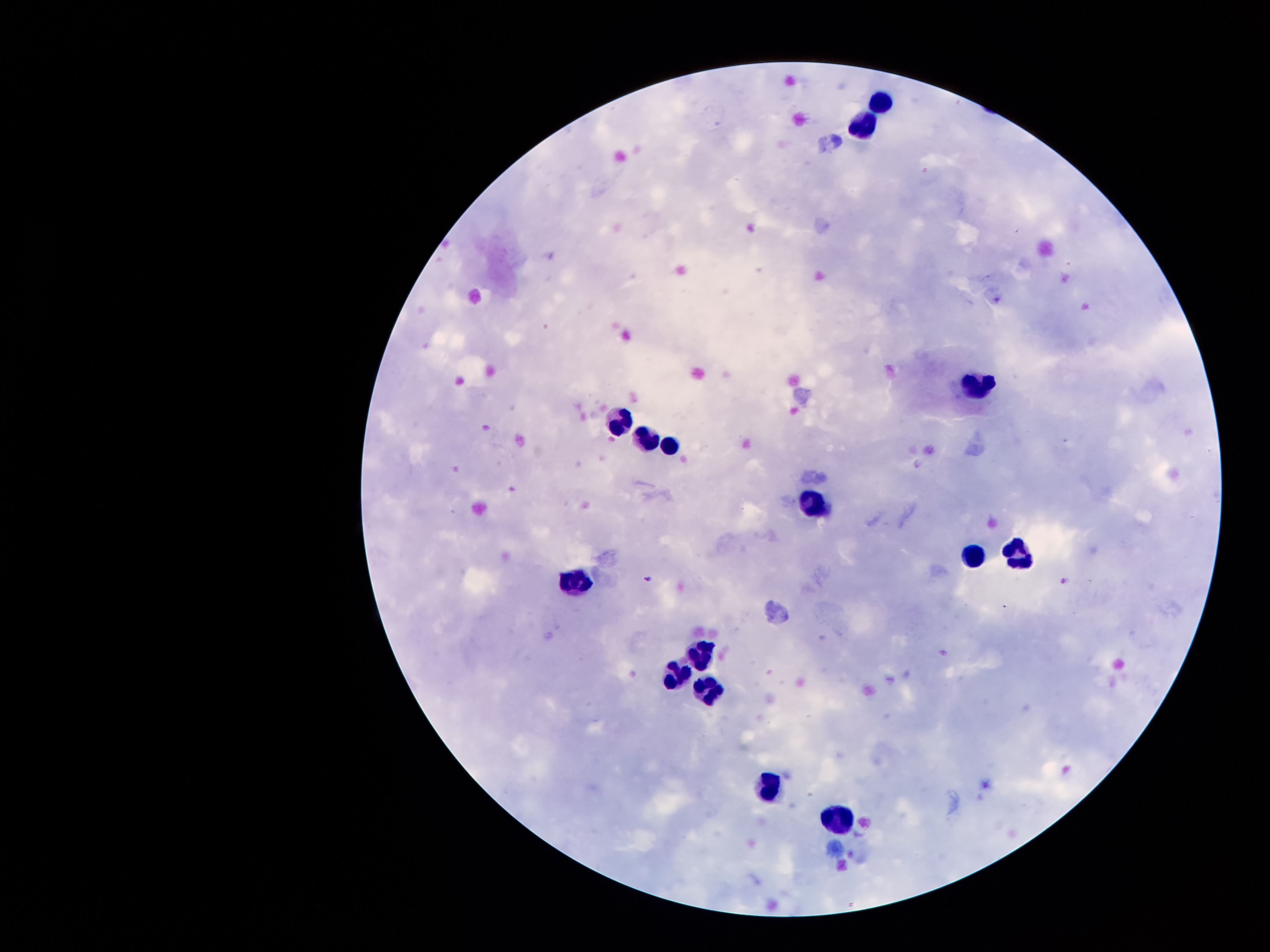

Approximate centers as {x, y} in pixels.
Summary:
  - Leukocyte locations: {880, 97}, {858, 123}, {979, 385}, {618, 423}, {650, 437}, {674, 444}, {814, 503}, {1021, 555}, {976, 557}, {579, 580}, {708, 653}, {675, 674}, {713, 692}, {767, 788}, {841, 818}
  - Malaria parasite locations: {647, 580}, {1063, 583}
  - Capture: smartphone camera through the microscope eyepiece
  - Magnification: 100x
  - Preparation: thick peripheral-blood smear
  - Patient malaria status: infected with Plasmodium falciparum
  - Stain: Giemsa
  - Field of view: single
  - Image size: 1270×952 pixels